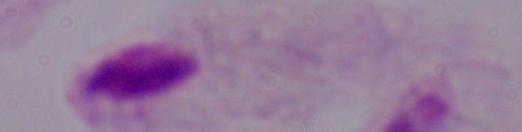

1000x magnification. Photomicrograph. A trichomonad is seen.